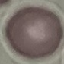

Result: no malaria parasites seen. Thin blood film. Acquired by smartphone through the microscope eyepiece. Cell patch, automatically extracted from a larger field of view and resized to 64 × 64 pixels. Giemsa-stained preparation.